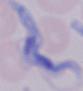

Summary:
  - Magnification: 1000x
  - Modality: photomicrograph
  - Identification: trypanosome